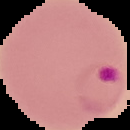

Image is 130×130 pixels. From a thin blood smear. Cell region segmented out of the field of view; the surrounding area is masked to black. Malaria status: parasitized.